Name the parasite shown.
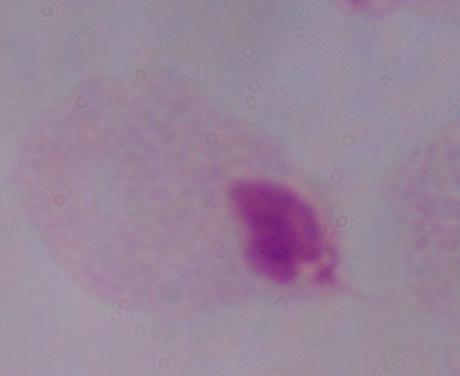
A trichomonad.

Summary:
  - Modality: photomicrograph
  - Magnification: 1000x